Comment on the morphology of the red blood cells.
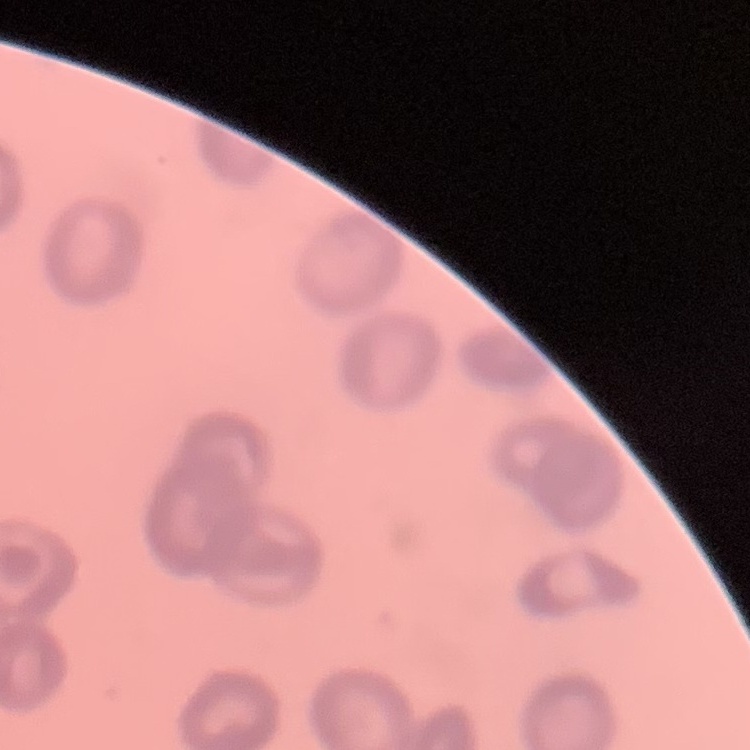
Rouleaux formation.

preparation = thin blood film
image type = square crop of a larger photomicrograph
stain = Field's or Giemsa